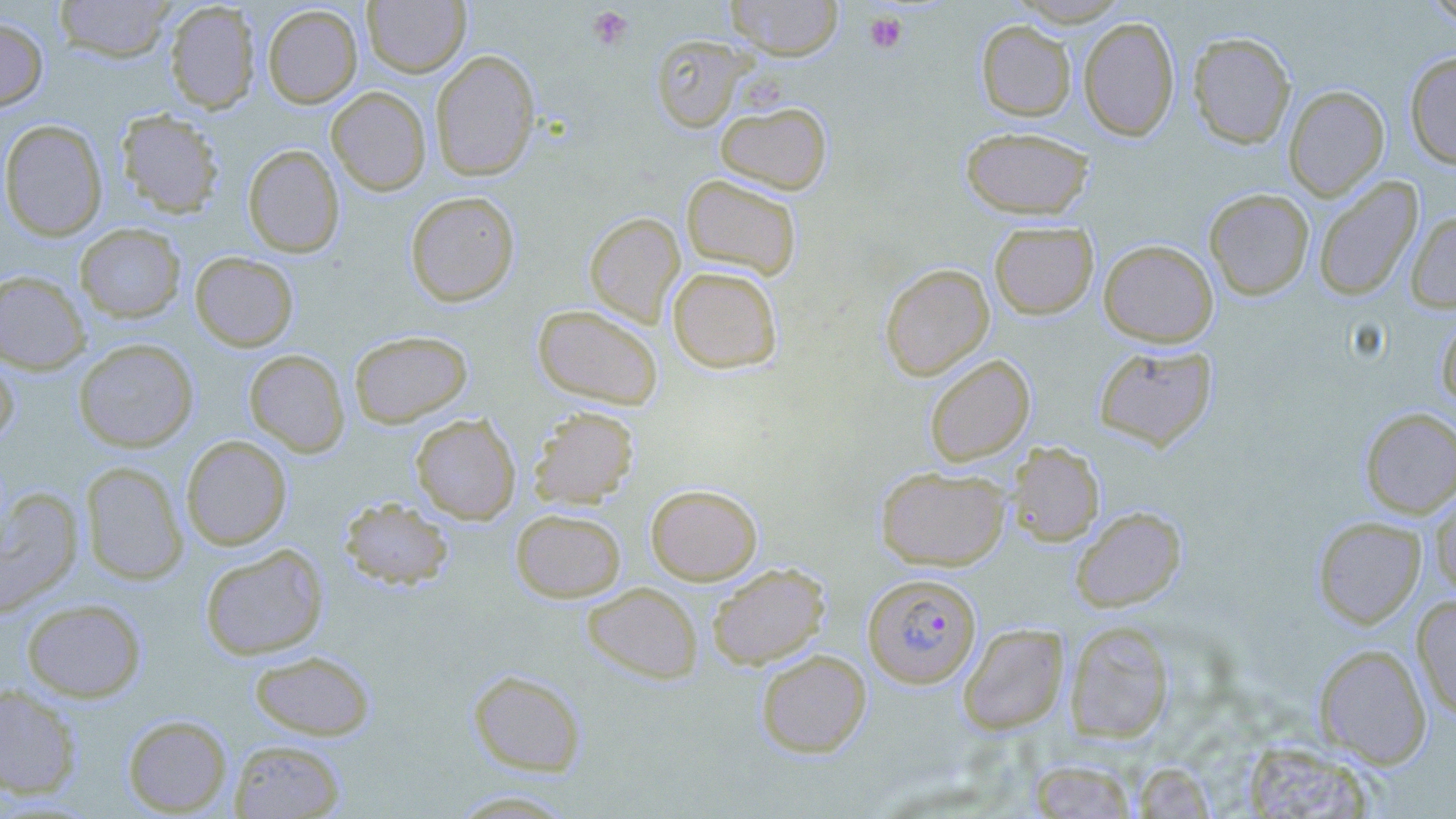

Approximate bounding boxes as (x1,y1)-(x2,y2) corner pairs in pixels. Platelet locations: (588,6)-(633,49), (865,12)-(907,53). Uninfected red blood cell locations: (53,0)-(176,63), (727,0)-(844,59), (1421,0)-(1456,28), (164,1)-(260,113), (363,1)-(470,77), (262,4)-(363,108), (1078,16)-(1180,141), (0,17)-(49,112), (976,20)-(1077,121), (1188,32)-(1296,148), (651,35)-(750,131), (430,49)-(541,181), (1405,51)-(1456,170), (1283,85)-(1389,200), (326,87)-(431,196), (715,101)-(832,194), (115,108)-(225,218), (0,119)-(108,241), (960,126)-(1095,219), (243,144)-(345,257), (681,174)-(803,281), (1313,176)-(1423,301), (1204,188)-(1314,300), (405,191)-(520,307), (1405,211)-(1456,314), (584,212)-(685,327), (989,221)-(1098,319), (75,223)-(186,323), (1098,239)-(1219,347), (189,251)-(299,351), (879,263)-(994,380), (667,265)-(783,374), (0,271)-(91,374), (532,304)-(663,410), (1435,312)-(1456,412), (349,330)-(472,428), (73,339)-(199,452), (1093,344)-(1217,451), (0,348)-(19,452), (244,349)-(349,457), (924,353)-(1035,467), (528,406)-(640,509), (1360,408)-(1456,519), (410,413)-(521,524), (181,435)-(292,550), (1007,441)-(1105,546), (80,461)-(188,585), (875,465)-(1010,571), (645,484)-(762,584), (0,487)-(84,616), (1429,487)-(1456,599), (338,496)-(454,590), (1070,506)-(1186,612), (511,508)-(626,602), (1313,516)-(1426,629), (199,543)-(328,660), (708,562)-(830,669), (582,582)-(704,684), (1412,595)-(1456,721), (21,597)-(147,702), (1064,620)-(1176,744), (958,622)-(1069,734), (1314,643)-(1432,769), (755,649)-(872,758), (249,650)-(375,740), (467,669)-(587,776), (0,685)-(83,800), (122,714)-(232,816), (228,738)-(347,818), (1241,740)-(1371,818), (1030,759)-(1137,818), (1134,762)-(1215,818), (446,789)-(582,817). Plasmodium falciparum-infected red blood cell locations: (862,572)-(982,688). Slide-level diagnosis: Plasmodium falciparum. Optical microscopy. 1000x magnification. Thin blood smear. May-Grünwald-Giemsa-stained preparation. Single field of view. Image is 1456×819 pixels.